Locate every Plasmodium falciparum-infected red blood cell.
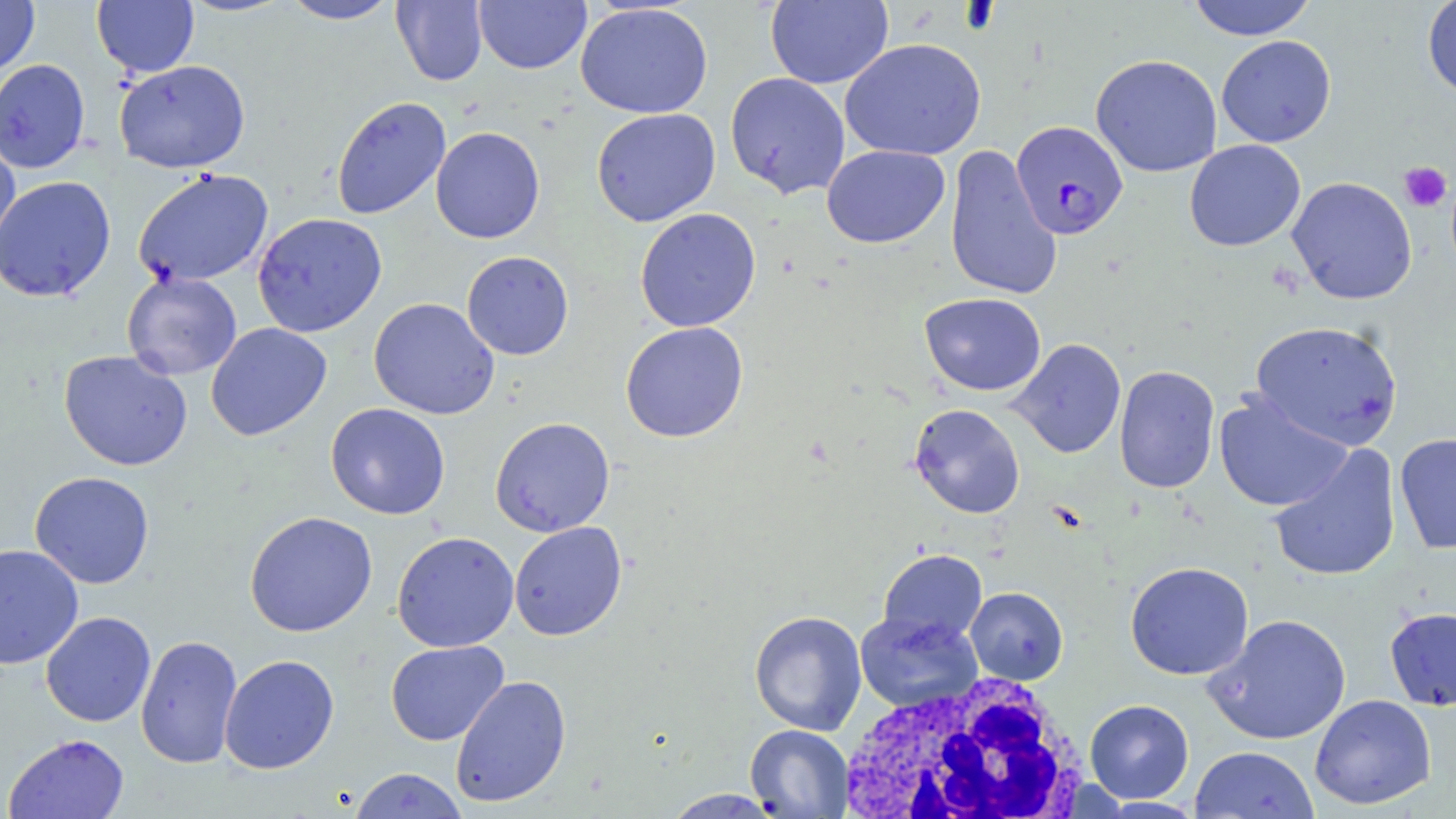
Approximate bounding boxes as [x1, y1, x2, y2] in pixels.
Plasmodium falciparum-infected red blood cells: [1010, 120, 1127, 240].

White blood cell locations: [833, 672, 1091, 819]. Platelet locations: [1398, 162, 1451, 213]. Uninfected red blood cell locations: [92, 0, 199, 77], [280, 0, 401, 24], [391, 0, 488, 86], [474, 0, 591, 74], [765, 0, 893, 89], [1185, 0, 1317, 41], [0, 1, 39, 79], [1421, 1, 1456, 100], [575, 2, 713, 119], [1216, 35, 1336, 147], [840, 38, 986, 161], [1090, 54, 1222, 178], [0, 59, 91, 174], [114, 60, 250, 173], [724, 72, 851, 199], [331, 96, 451, 220], [591, 108, 720, 227], [430, 126, 545, 244], [0, 129, 21, 260], [1184, 139, 1305, 252], [821, 144, 950, 249], [944, 144, 1062, 301], [133, 168, 274, 289], [0, 175, 116, 302], [1286, 176, 1417, 305], [634, 208, 761, 333], [252, 212, 387, 337], [461, 251, 574, 360], [121, 272, 242, 380], [920, 292, 1046, 396], [368, 297, 500, 420], [1250, 320, 1403, 451], [205, 322, 332, 441], [620, 322, 749, 443], [1008, 338, 1127, 459], [59, 350, 193, 471], [1114, 365, 1220, 494], [1213, 390, 1353, 513], [325, 402, 451, 520], [908, 403, 1025, 519], [489, 416, 615, 537], [1394, 432, 1456, 554], [1268, 444, 1402, 582], [29, 471, 155, 589], [244, 511, 378, 637], [508, 521, 628, 641], [392, 531, 519, 652], [0, 544, 84, 670], [878, 548, 988, 646], [1125, 561, 1254, 680], [965, 587, 1068, 685], [1384, 606, 1456, 711], [749, 610, 867, 735], [40, 611, 156, 727], [854, 611, 983, 712], [1204, 613, 1352, 745], [135, 634, 243, 770], [385, 640, 509, 746], [219, 654, 340, 774], [450, 675, 572, 807], [1309, 694, 1436, 810], [1084, 699, 1195, 803], [745, 725, 854, 818], [3, 733, 130, 818], [1189, 745, 1319, 818], [348, 767, 470, 818], [662, 789, 786, 818]. Slide-level diagnosis: Plasmodium falciparum. May-Grünwald-Giemsa-stained preparation. Captured at 1000x magnification. Image is 1456×819 pixels. Single field of view. Thin blood smear. Optical microscopy.